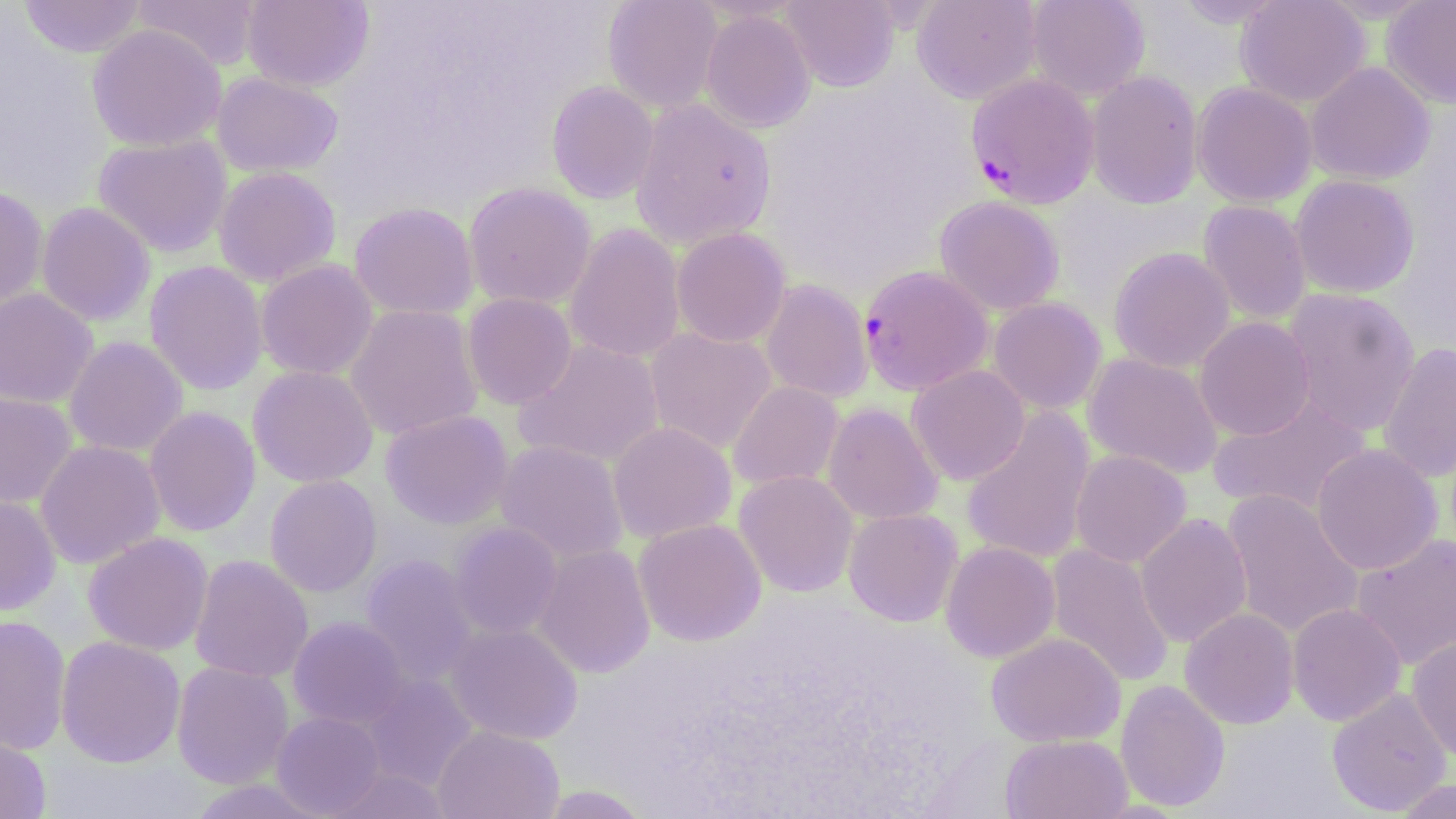
slide_level_diagnosis: Plasmodium falciparum
stain: May-Grünwald-Giemsa
field_of_view: one of a larger specimen
image_size: 1456×819 pixels
uninfected_red_blood_cell_locations: 'approximate bounding boxes as (x1,y1)-(x2,y2) corner pairs in pixels: (19,0)-(147,58), (242,0)-(374,91), (602,0)-(723,112), (780,0)-(900,92), (911,0)-(1042,104), (1026,0)-(1150,101), (1235,0)-(1371,107), (1381,0)-(1456,109), (132,1)-(261,71), (700,9)-(817,134), (87,24)-(226,151), (1306,62)-(1435,185), (212,71)-(343,178), (1086,71)-(1203,210), (546,81)-(659,204), (1192,82)-(1317,207), (629,99)-(777,248), (92,134)-(232,258), (213,166)-(342,286), (1290,174)-(1420,298), (463,182)-(596,310), (0,186)-(48,313), (934,196)-(1065,316), (1198,200)-(1311,324), (36,202)-(156,326), (349,202)-(479,319), (564,223)-(685,364), (671,227)-(790,348), (1108,247)-(1235,373), (255,259)-(378,380), (144,260)-(268,395), (759,278)-(873,404), (1281,287)-(1420,437), (0,288)-(97,409), (461,293)-(577,409), (988,297)-(1107,414), (345,303)-(483,441), (1194,316)-(1315,441), (645,327)-(777,455), (63,336)-(188,457), (513,340)-(665,468), (1377,343)-(1456,483), (1083,353)-(1223,479), (248,365)-(378,487), (907,365)-(1030,485), (728,381)-(844,490), (0,390)-(78,509), (1207,395)-(1372,517), (822,402)-(943,525), (144,406)-(261,537), (961,407)-(1096,566), (380,409)-(514,529), (608,421)-(736,543), (35,439)-(165,568), (494,440)-(629,565), (1312,443)-(1442,575), (1070,449)-(1191,567), (734,470)-(859,597), (264,475)-(383,597), (1220,489)-(1364,640), (0,494)-(60,616), (843,508)-(963,627), (1135,513)-(1252,648), (633,518)-(766,646), (449,522)-(562,639), (83,532)-(213,655), (1351,532)-(1456,671), (940,541)-(1060,662), (533,544)-(655,678), (1046,544)-(1174,687), (189,554)-(313,683), (361,555)-(479,684), (1288,603)-(1406,726), (1179,607)-(1299,729), (0,615)-(71,755), (288,617)-(411,729), (445,622)-(583,744), (986,632)-(1125,747), (56,635)-(186,768), (1407,637)-(1456,762), (172,661)-(294,788), (359,673)-(478,791), (1115,680)-(1230,812), (1326,687)-(1452,816), (271,711)-(386,817), (433,724)-(564,819), (0,729)-(51,819), (1000,734)-(1134,819), (324,767)-(452,818), (1391,778)-(1456,818), (537,785)-(654,819)'
plasmodium_falciparum_infected_red_blood_cell_locations: 'approximate bounding boxes as (x1,y1)-(x2,y2) corner pairs in pixels: (966,73)-(1099,208), (858,265)-(992,395)'
magnification: 1000x
modality: optical microscopy
preparation: thin blood film